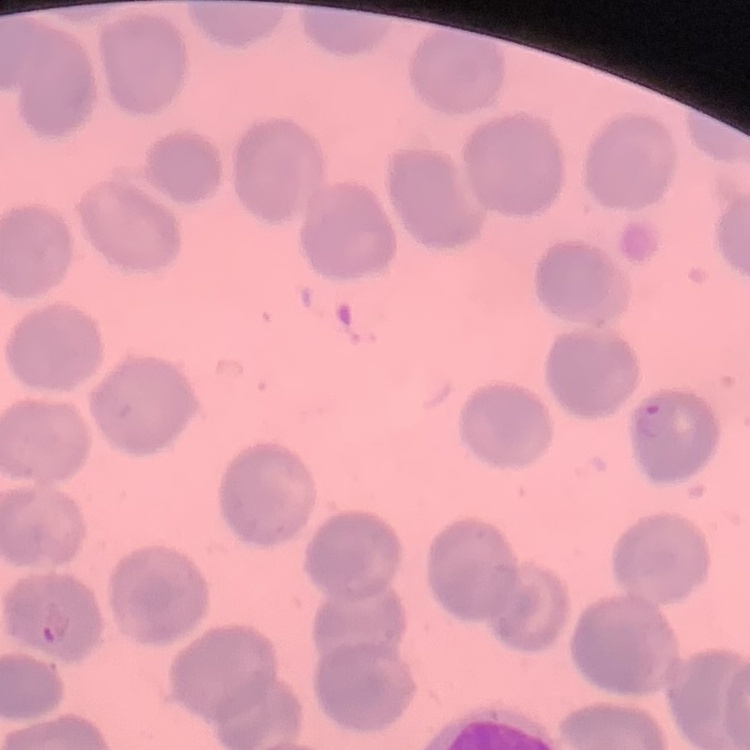

erythrocyte morphology = no rouleaux formation
stain = Field's or Giemsa
preparation = thin blood film
image type = square crop of a larger photomicrograph